Which red blood cells are P. falciparum-infected, and which are of indeterminate infection status?
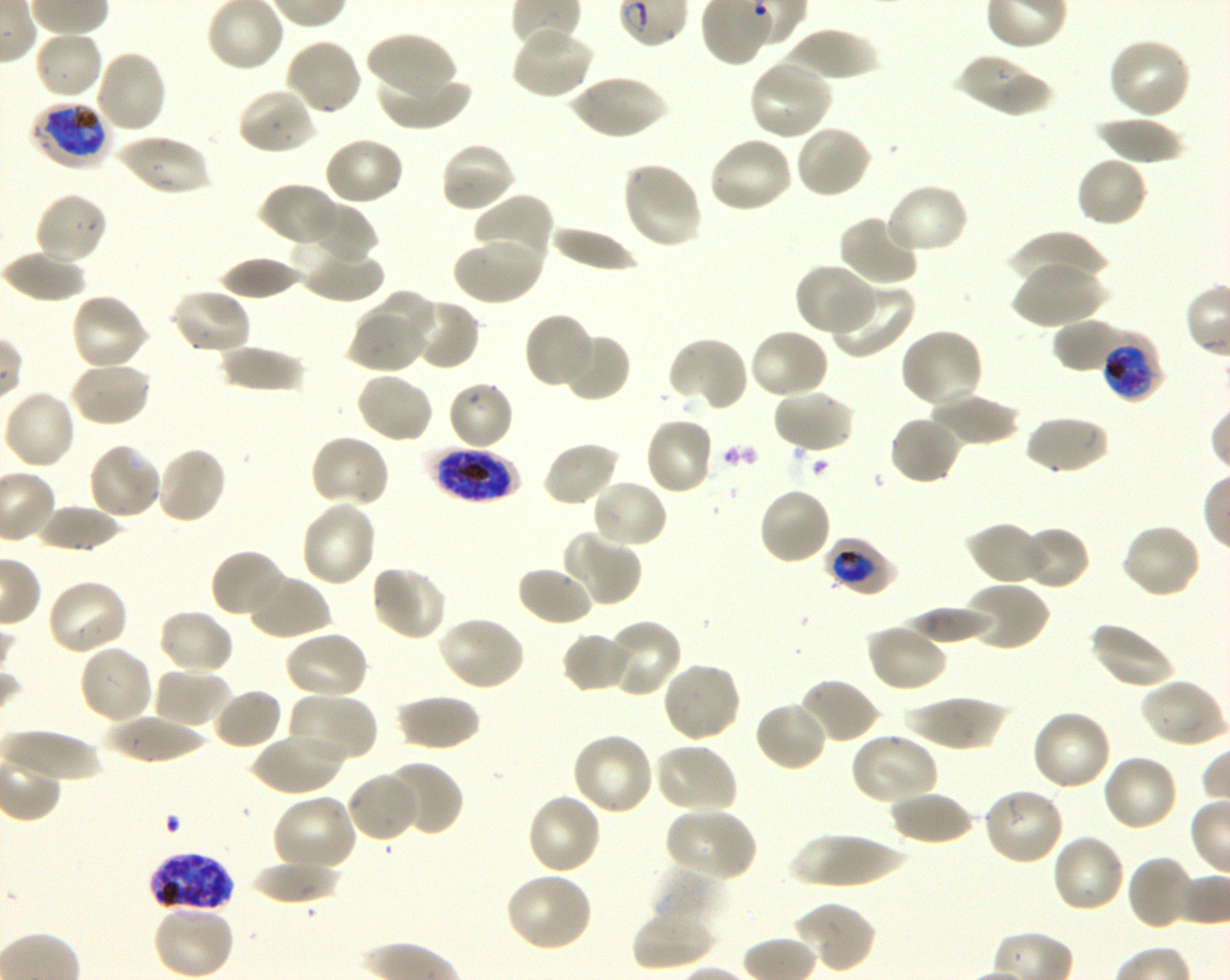
Approximate bounding boxes as {x1, y1, x2, y2} in pixels. Not every red blood cell is marked. A life-cycle stage — or a range of stages, where the recorded stages span more than one — follows each staged infected red blood cell.
Infected red blood cells: {29, 99, 113, 171} early trophozoite to early schizont; {1099, 335, 1162, 401} early trophozoite to early schizont; {430, 446, 520, 502} late trophozoite to late schizont; {826, 537, 899, 597} trophozoite; {147, 850, 233, 916} schizont.
No red blood cells of indeterminate infection status observed.

Summary:
  - Locations of uninfected red blood cells: {510, 25, 595, 101}, {34, 29, 104, 101}, {783, 29, 881, 81}, {366, 32, 460, 106}, {284, 37, 363, 116}, {1107, 37, 1193, 120}, {94, 49, 169, 135}, {957, 52, 1053, 118}, {748, 59, 833, 142}, {375, 72, 472, 130}, {565, 74, 670, 140}, {236, 87, 315, 156}, {1093, 116, 1190, 164}, {794, 124, 872, 199}, {114, 134, 211, 196}, {323, 135, 405, 207}, {707, 135, 793, 215}, {438, 141, 516, 214}, {1075, 155, 1150, 228}, {621, 161, 703, 250}, {884, 182, 969, 256}, {258, 183, 342, 248}, {34, 192, 109, 267}, {473, 193, 553, 273}, {301, 203, 378, 267}, {839, 213, 920, 286}, {548, 224, 641, 271}, {1007, 231, 1109, 286}, {453, 237, 542, 305}, {297, 246, 387, 303}, {0, 249, 88, 301}, {218, 256, 302, 300}, {1012, 260, 1106, 329}, {795, 263, 876, 337}, {826, 283, 915, 360}, {169, 287, 251, 355}, {372, 290, 436, 347}, {69, 292, 150, 372}, {399, 299, 481, 371}, {349, 308, 427, 373}, {522, 311, 595, 390}, {1054, 319, 1131, 375}, {899, 327, 985, 410}, {747, 328, 830, 401}, {558, 330, 632, 403}, {667, 336, 749, 412}, {217, 344, 304, 394}, {69, 361, 153, 428}, {355, 370, 435, 445}, {447, 380, 514, 451}, {2, 389, 76, 470}, {772, 389, 855, 454}, {928, 393, 1022, 448}, {888, 414, 964, 486}, {1024, 414, 1108, 476}, {644, 416, 716, 496}, {309, 435, 391, 509}, {541, 440, 621, 508}, {87, 443, 163, 522}, {155, 445, 228, 526}, {590, 479, 669, 549}, {757, 486, 834, 566}, {299, 500, 378, 587}, {34, 504, 126, 552}, {965, 521, 1046, 586}, {1120, 523, 1203, 599}, {1019, 525, 1090, 590}, {564, 532, 640, 604}, {210, 548, 286, 621}, {370, 563, 448, 642}, {516, 564, 594, 627}, {246, 572, 330, 641}, {44, 578, 130, 656}, {964, 582, 1049, 653}, {901, 606, 993, 646}, {157, 608, 236, 676}, {437, 614, 526, 692}, {605, 619, 683, 698}, {1089, 621, 1177, 690}, {866, 622, 948, 693}, {283, 629, 370, 702}, {562, 632, 636, 694}, {77, 643, 154, 725}, {660, 659, 742, 743}, {152, 667, 232, 730}, {796, 676, 880, 745}, {1139, 676, 1226, 748}, {211, 688, 283, 751}, {287, 693, 377, 766}, {395, 693, 480, 751}, {902, 695, 1010, 751}, {754, 699, 827, 773}, {1031, 708, 1113, 791}, {103, 715, 208, 764}, {1, 728, 106, 781}, {252, 730, 345, 796}, {850, 731, 939, 806}, {570, 732, 654, 817}, {652, 742, 739, 815}, {1100, 753, 1179, 832}, {380, 759, 463, 837}, {347, 772, 420, 843}, {982, 786, 1066, 866}, {890, 789, 975, 846}, {525, 792, 603, 877}, {272, 793, 358, 873}, {665, 807, 757, 882}, {787, 832, 910, 888}, {1050, 833, 1127, 914}, {1126, 855, 1198, 931}, {248, 861, 343, 904}, {649, 868, 725, 929}, {505, 872, 594, 953}, {792, 900, 877, 973}, {152, 903, 235, 980}, {632, 907, 715, 972}
  - Life-cycle stages observed: trophozoite, schizont
  - Stain: Giemsa
  - Culture: in-vitro P. falciparum strain 3D7, shaking
  - Objective: 100x, oil immersion, numerical aperture 1.30
  - Field of view: one from this slide
  - Image size: 1230×980 pixels
  - Donor blood group: O+
  - Preparation: thin blood film